State which parasite is depicted.
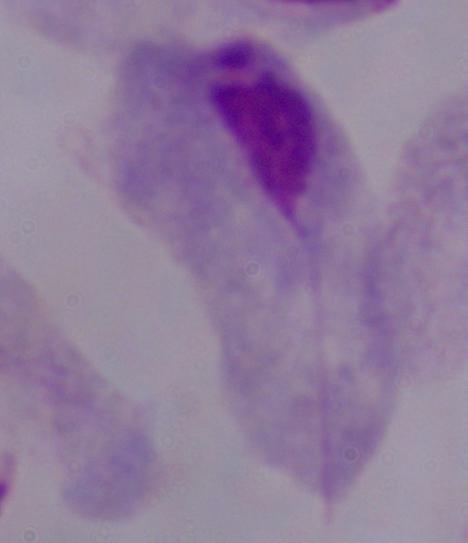
This is a trichomonad.

1000x magnification. Micrograph.